Evaluate for Plasmodium parasites.
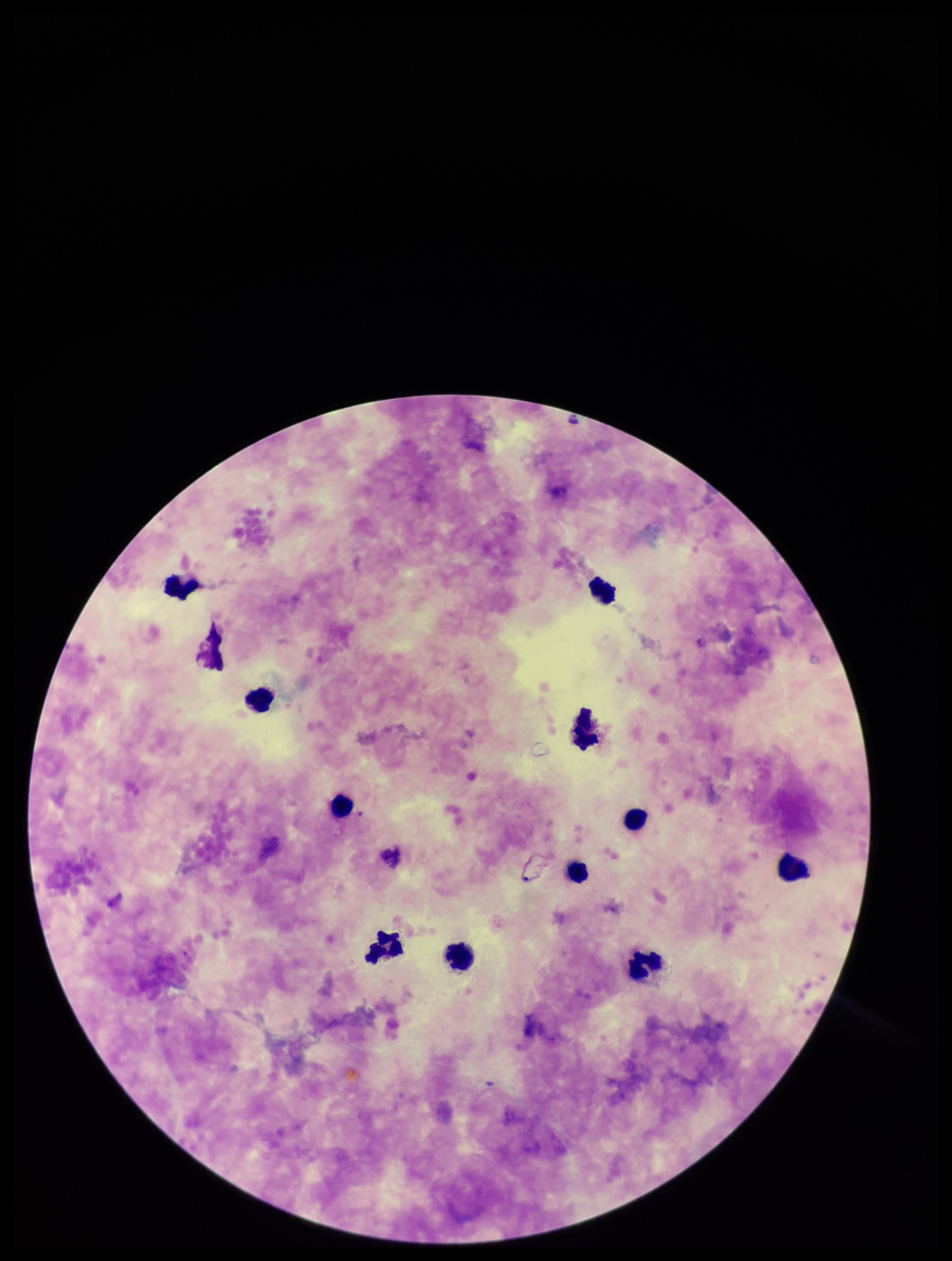

None detected.

Summary:
  - Stain: Giemsa
  - Patient malaria status: negative
  - Parasite count: 0
  - Field of view: one from this slide
  - Image size: 952×1261 pixels
  - Leukocyte count: 11
  - Capture: smartphone photograph through the microscope eyepiece
  - Preparation: thick smear